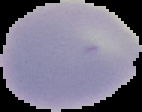
Summary:
  - Image type: segmented cell region on a black background
  - Preparation: thin blood smear
  - Result: negative for Plasmodium parasites
  - Image size: 142×112 pixels